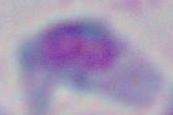
identification = Toxoplasma gondii
modality = photomicrograph
magnification = 1000x